Outline platelets.
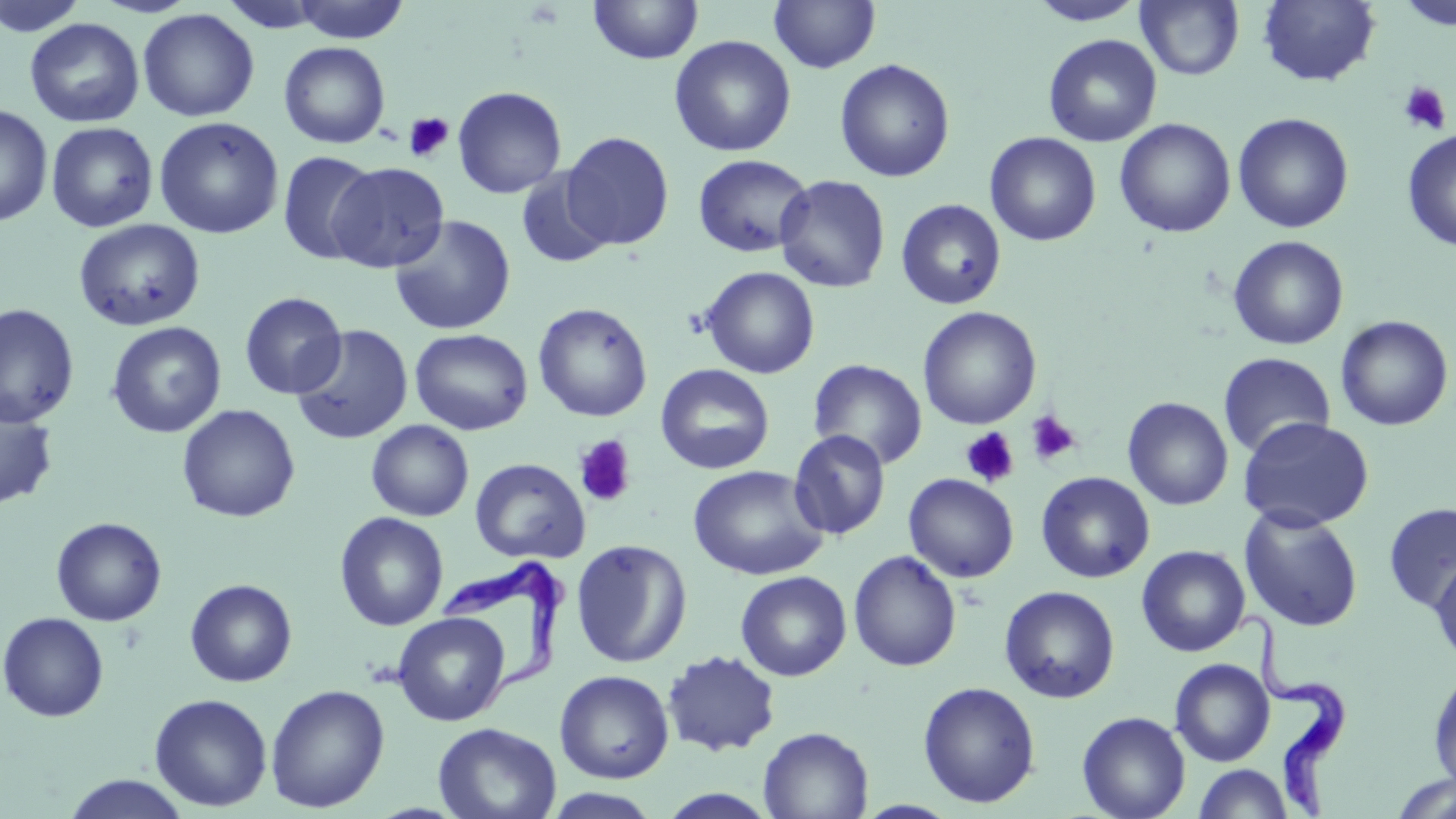

Approximate bounding boxes as [x1, y1, x2, y2] in pixels.
Platelets: [1399, 81, 1451, 135], [403, 112, 454, 163], [1026, 410, 1081, 466], [960, 427, 1019, 487], [573, 435, 637, 508].

slide_level_diagnosis: Trypanosoma brucei
modality: optical microscopy
trypanosoma_brucei_locations: 'approximate bounding boxes as [x1, y1, x2, y2] in pixels: [438, 557, 566, 687], [1236, 610, 1351, 817]'
uninfected_red_blood_cell_locations: 'approximate bounding boxes as [x1, y1, x2, y2] in pixels: [0, 0, 91, 38], [289, 0, 410, 43], [588, 0, 703, 65], [769, 0, 880, 73], [1027, 0, 1149, 26], [1136, 0, 1244, 81], [1258, 0, 1381, 87], [1394, 0, 1456, 31], [137, 8, 260, 122], [25, 18, 144, 128], [1043, 33, 1162, 147], [669, 35, 796, 157], [278, 41, 391, 149], [834, 58, 955, 183], [452, 86, 567, 198], [0, 103, 54, 227], [1232, 113, 1354, 233], [153, 116, 284, 239], [1115, 118, 1236, 238], [46, 121, 158, 232], [1402, 128, 1456, 252], [560, 131, 674, 251], [985, 132, 1101, 247], [278, 150, 378, 264], [693, 154, 814, 257], [326, 162, 450, 273], [515, 167, 616, 269], [774, 174, 891, 293], [896, 198, 1007, 310], [389, 215, 516, 335], [74, 218, 205, 332], [1228, 235, 1349, 350], [700, 266, 820, 379], [239, 292, 348, 399], [0, 303, 80, 428], [533, 303, 653, 422], [917, 306, 1042, 429], [1335, 315, 1453, 431], [106, 321, 227, 438], [291, 324, 414, 445], [410, 328, 533, 435], [1218, 351, 1336, 458], [808, 359, 928, 469], [655, 364, 775, 475], [0, 395, 59, 511], [1122, 396, 1233, 510], [177, 404, 301, 523], [1238, 416, 1374, 532], [366, 419, 474, 521], [788, 429, 891, 540], [470, 458, 590, 564], [688, 464, 828, 580], [1036, 471, 1155, 583], [903, 473, 1019, 582], [1383, 503, 1456, 613], [1239, 506, 1364, 632], [334, 511, 449, 631], [51, 517, 167, 626], [571, 539, 692, 668], [1136, 545, 1251, 656], [849, 550, 962, 671], [1429, 557, 1456, 669], [735, 570, 852, 681], [184, 579, 298, 687], [999, 585, 1120, 703], [1, 612, 109, 722], [392, 612, 510, 726], [661, 650, 781, 756], [1170, 658, 1275, 766], [1428, 668, 1456, 791], [554, 670, 675, 782], [917, 680, 1041, 807], [265, 684, 390, 813], [150, 693, 272, 811], [1077, 710, 1191, 819], [433, 722, 562, 818], [758, 726, 873, 818], [1193, 764, 1294, 819], [62, 773, 192, 818], [1390, 774, 1456, 818], [543, 788, 663, 819], [656, 789, 781, 818]'
stain: May-Grünwald-Giemsa
preparation: thin blood smear
magnification: 1000x
field_of_view: single
image_size: 1456×819 pixels